Assess this cell for malaria.
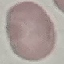

Uninfected.

Giemsa-stained preparation. Photographed with a smartphone camera at the microscope eyepiece. Automatically extracted cell patch, resized to 64 × 64 pixels. Thin smear of blood.